Assess this cell for malaria.
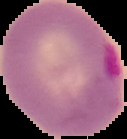

It is parasitized.

Segmented cell region on a black background. Image is 127×139 pixels. From a thin blood smear.